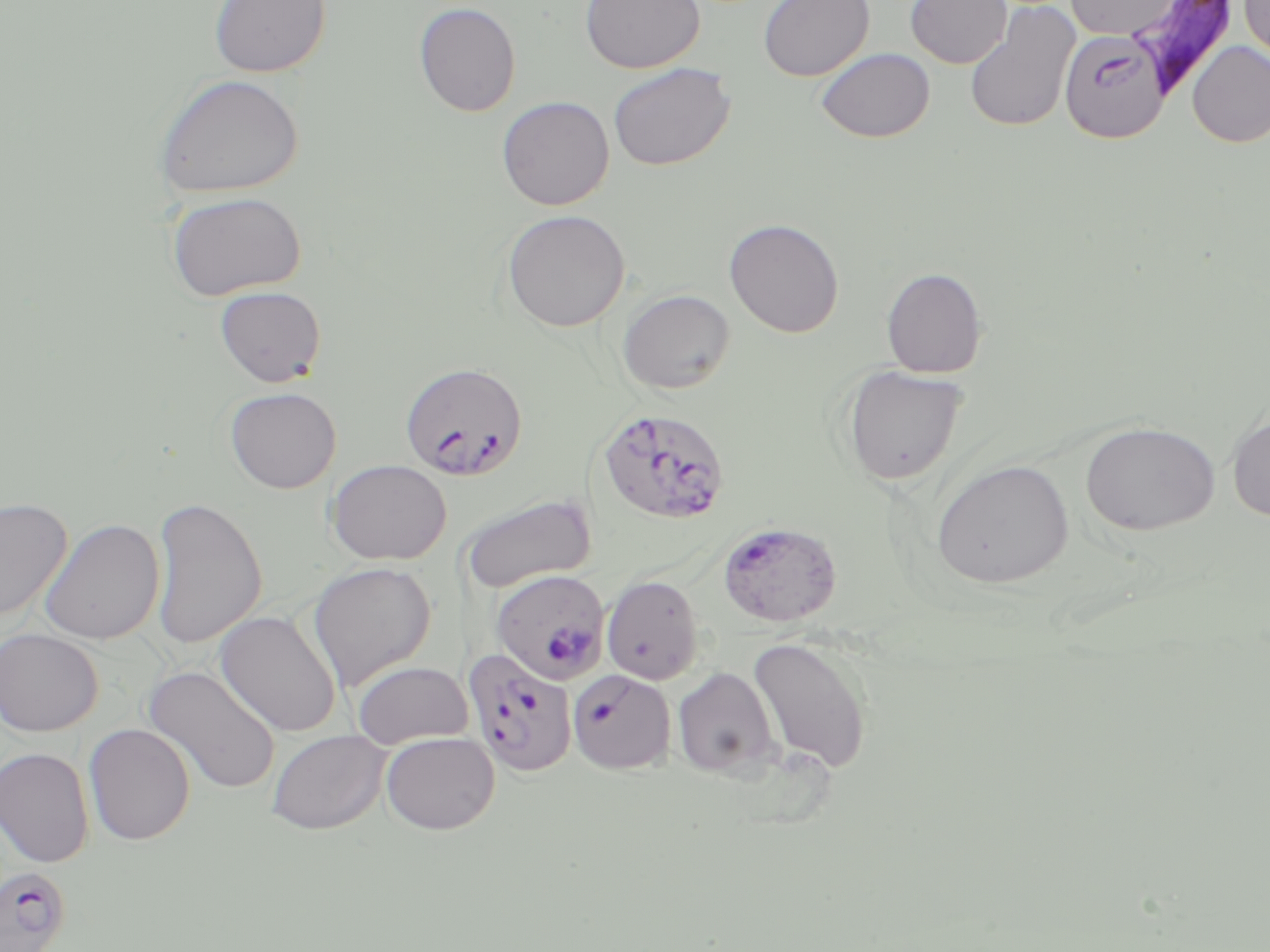
plasmodium_falciparum_infected_red_blood_cell_locations: 'approximate bounding boxes as (x1, y1, x2, y2) in pixels: (1063, 32, 1175, 147), (399, 360, 528, 481), (595, 407, 731, 525), (718, 520, 842, 627), (490, 568, 611, 684), (462, 648, 578, 778), (567, 669, 676, 774), (0, 868, 73, 952)'
slide_level_diagnosis: Plasmodium falciparum
image_size: 1270×952 pixels
stain: May-Grünwald-Giemsa
field_of_view: one of a larger specimen
uninfected_red_blood_cell_locations: 'approximate bounding boxes as (x1, y1, x2, y2) in pixels: (208, 0, 331, 78), (579, 0, 706, 74), (758, 0, 874, 82), (905, 0, 1012, 68), (1065, 0, 1181, 38), (1239, 0, 1270, 68), (963, 1, 1081, 134), (413, 2, 521, 117), (1124, 6, 1246, 102), (1187, 41, 1270, 148), (815, 47, 935, 143), (608, 62, 735, 172), (153, 73, 304, 199), (496, 96, 615, 211), (166, 190, 307, 301), (501, 209, 631, 332), (723, 218, 844, 338), (881, 267, 987, 378), (214, 286, 326, 387), (617, 288, 735, 394), (840, 365, 969, 484), (224, 386, 342, 493), (1227, 413, 1270, 523), (1080, 420, 1221, 535), (326, 459, 452, 565), (931, 459, 1073, 588), (460, 493, 596, 593), (150, 496, 267, 650), (0, 498, 73, 622), (39, 518, 165, 645), (307, 562, 436, 691), (601, 574, 704, 685), (215, 611, 342, 737), (0, 629, 103, 736), (747, 636, 873, 774), (352, 661, 474, 746), (143, 665, 281, 794), (672, 667, 780, 778), (83, 723, 196, 845), (267, 729, 390, 834), (381, 732, 500, 834), (0, 747, 94, 868)'
magnification: 1000x
preparation: thin blood smear
modality: light microscopy